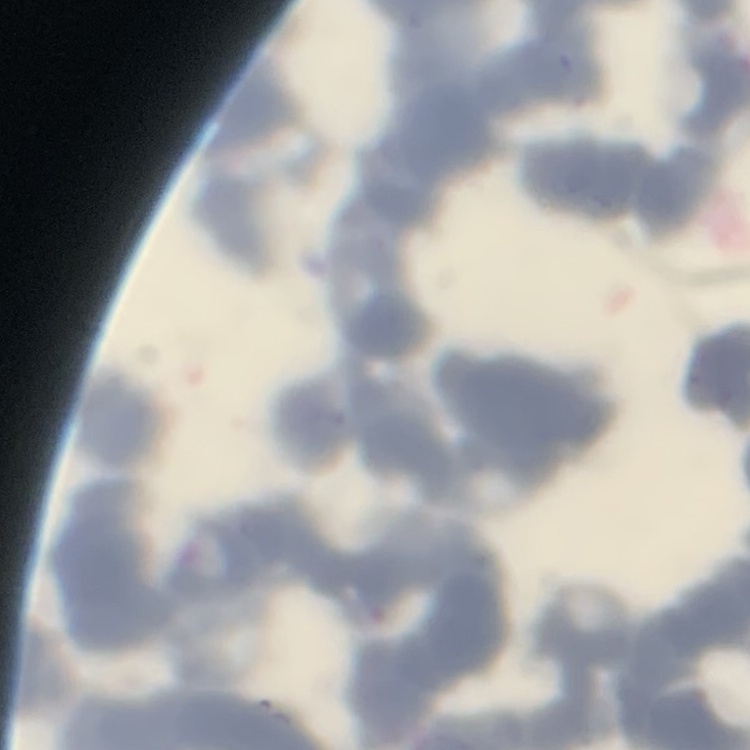
erythrocyte_morphology: rouleaux formation
image_type: one tile cut from a larger photomicrograph
stain: Field's or Giemsa
preparation: thin peripheral smear